Name the parasite shown.
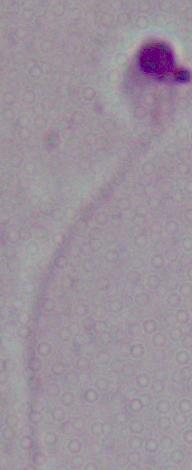
Leishmania.

Photomicrograph. Captured at 1000x magnification.